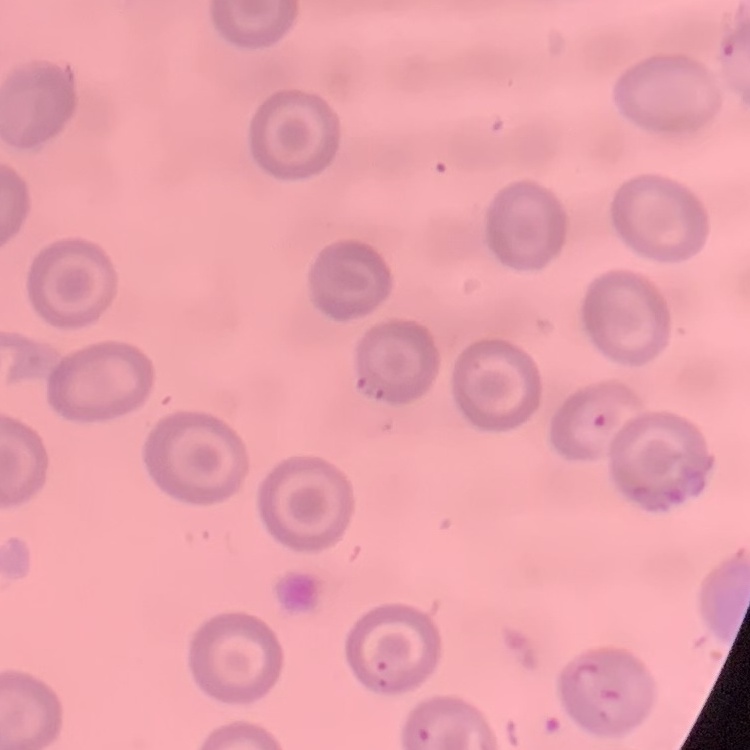
erythrocyte morphology = no rouleaux formation
image type = one tile cut from a larger photomicrograph
stain = Field's or Giemsa
preparation = thin blood film